Assess the morphology of the erythrocytes.
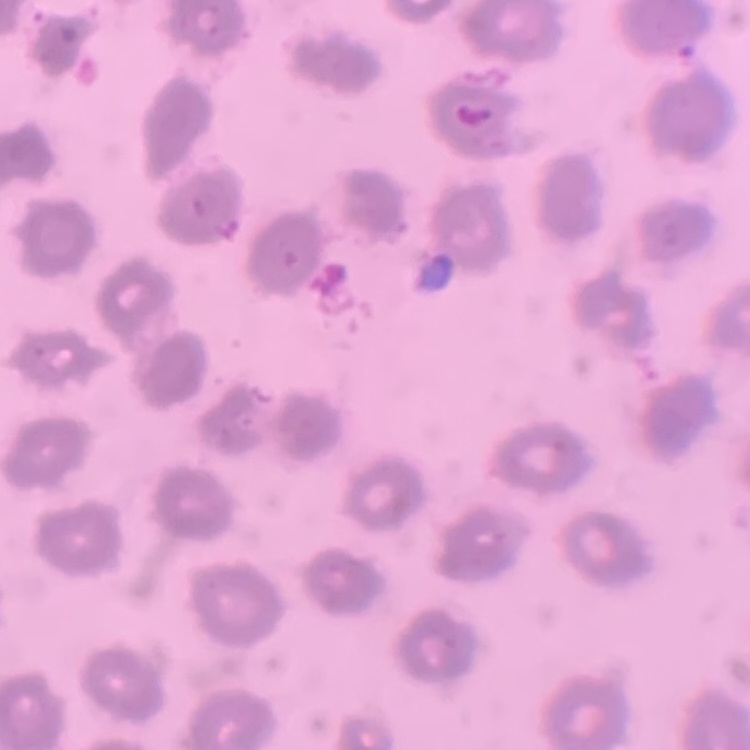
No rouleaux formation.

image type = one tile cut from a larger photomicrograph
stain = Field's or Giemsa
preparation = thin blood smear